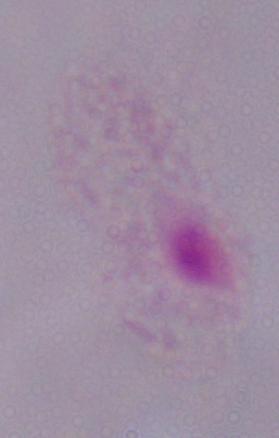

A trichomonad is shown. Micrograph. Captured at 1000x magnification.